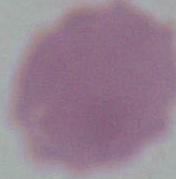

Summary:
  - Identification: erythrocyte
  - Modality: micrograph
  - Magnification: 1000x